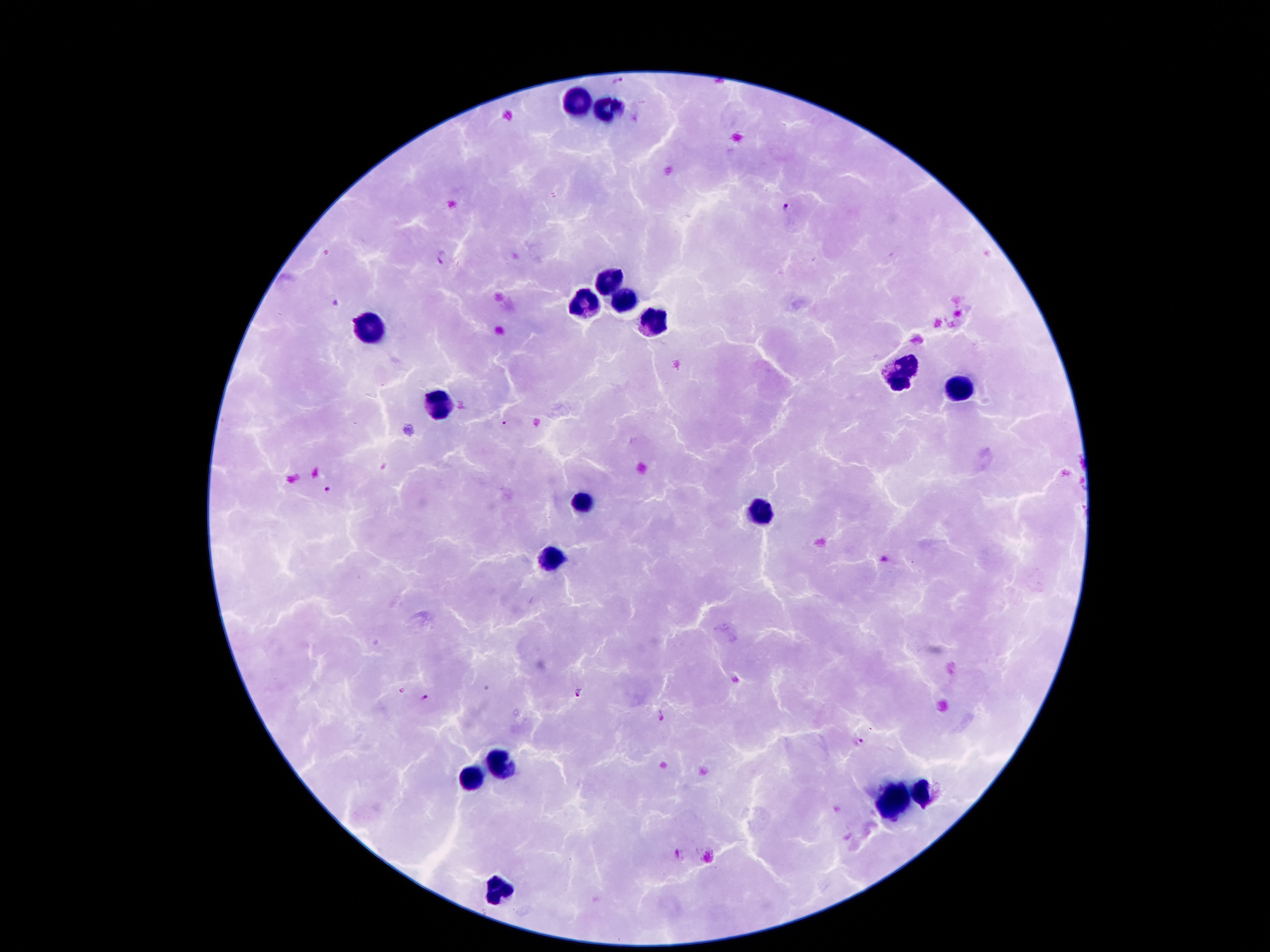
{
  "field_of_view": "single",
  "image_size": "1270×952 pixels",
  "patient_malaria_status": "positive for Plasmodium falciparum",
  "magnification": "100x",
  "stain": "Giemsa",
  "capture": "smartphone through the microscope eyepiece",
  "plasmodium_parasite_locations": "approximate object centers, in pixels from the top-left corner: (x=618, y=83), (x=788, y=206), (x=443, y=258), (x=331, y=302), (x=504, y=425), (x=326, y=491), (x=577, y=693), (x=425, y=699), (x=662, y=718), (x=858, y=743), (x=677, y=854)",
  "preparation": "thick peripheral-blood smear",
  "leukocyte_locations": "approximate object centers, in pixels from the top-left corner: (x=580, y=102), (x=607, y=109), (x=605, y=281), (x=584, y=304), (x=623, y=304), (x=648, y=320), (x=369, y=325), (x=900, y=379), (x=961, y=388), (x=439, y=411), (x=582, y=504), (x=762, y=513), (x=550, y=561), (x=500, y=765), (x=471, y=776), (x=923, y=790), (x=893, y=801), (x=496, y=892)"
}